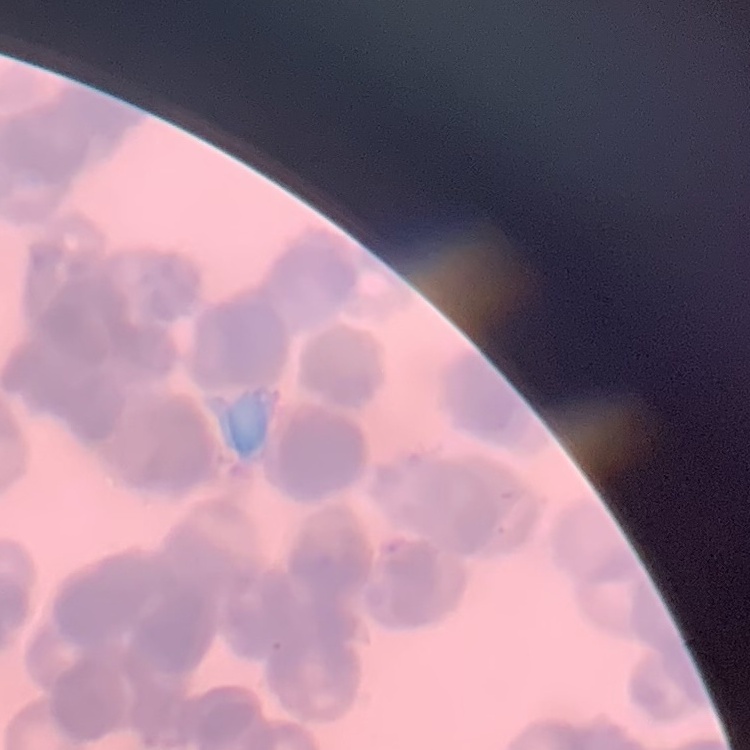

Summary:
  - Erythrocyte morphology: rouleaux formation
  - Image type: one tile cut from a larger photomicrograph
  - Preparation: thin peripheral smear
  - Stain: Field's or Giemsa